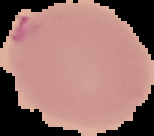 Malaria status: parasitized. Image is 154×136 pixels. From a thin blood film. The area outside the segmented cell region is set to black.